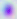

magnification = 400x
identification = Toxoplasma gondii
modality = photomicrograph